Describe the morphology of the red blood cells.
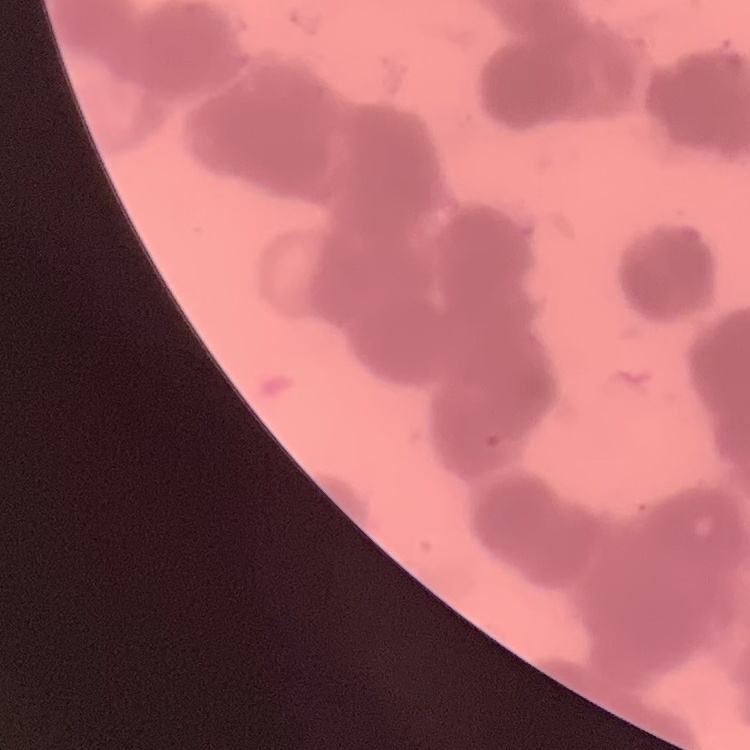
They show rouleaux formation.

Summary:
  - Image type: one tile cut from a larger photomicrograph
  - Preparation: thin blood smear
  - Stain: Field's or Giemsa